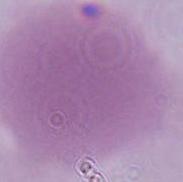

modality: photomicrograph
identification: erythrocyte
magnification: 1000x